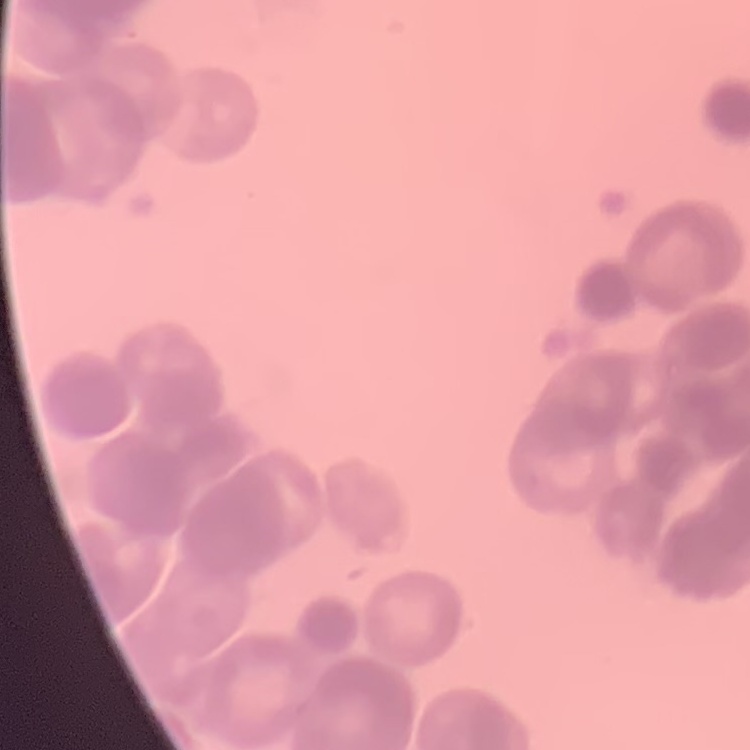

The erythrocytes exhibit rouleaux formation. Thin blood smear. Field's or Giemsa stain. One tile cut from a larger photomicrograph.